Rate the background quality.
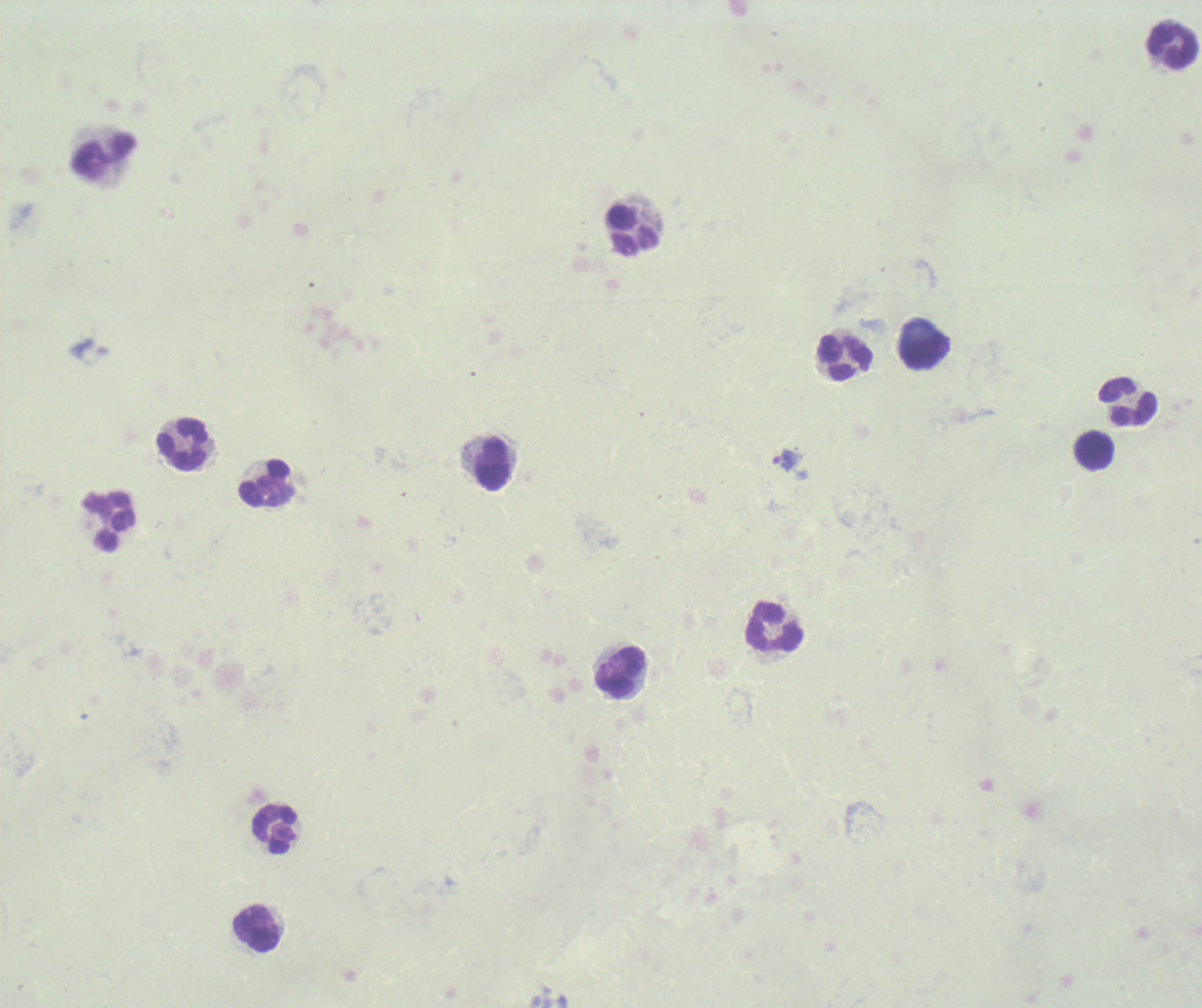
Unsatisfactory.

Approximate centers as (x, y) in pixels. Leukocyte locations: (1172, 45), (105, 158), (633, 230), (924, 351), (845, 358), (1127, 402), (182, 444), (1095, 450), (493, 462), (266, 484), (110, 522), (774, 627), (620, 671), (273, 829), (256, 928). Trophozoite locations: (786, 460). Result: positive for malaria parasites. 100x magnification. Thick blood film. Previously used in an actual diagnosis. Image is 1202×1008 pixels. One field from this slide. Romanowsky stain.